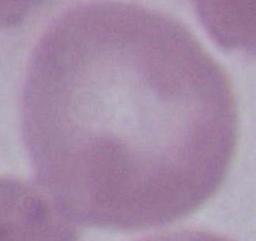
Summary:
  - Identification: red blood cell
  - Modality: photomicrograph
  - Magnification: 1000x